Report the malaria status.
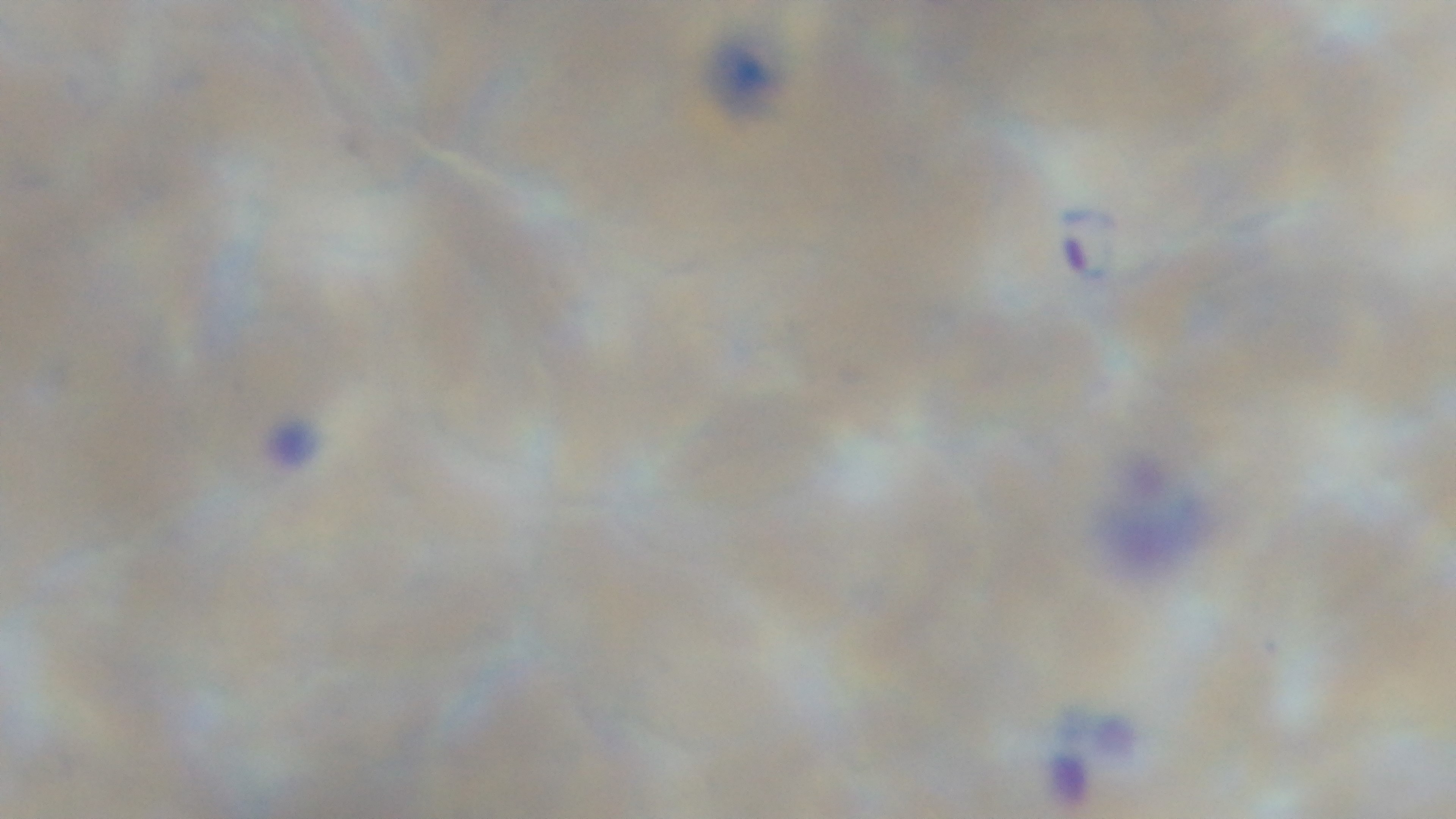

It is infected.

Summary:
  - Preparation: thin
  - Objective: 100x oil immersion
  - Capture: mounted 4K digital camera
  - Modality: light microscopy
  - Field of view: one from the slide
  - Stain: Giemsa